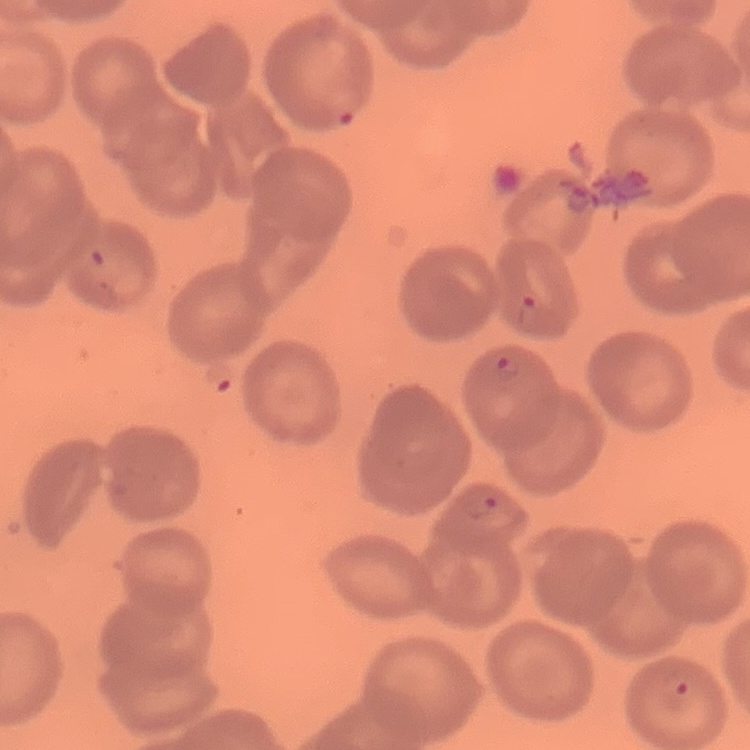 The red blood cells show no rouleaux formation. Thin peripheral smear. Stained with either Field's or Giemsa. Square crop of a larger photomicrograph.